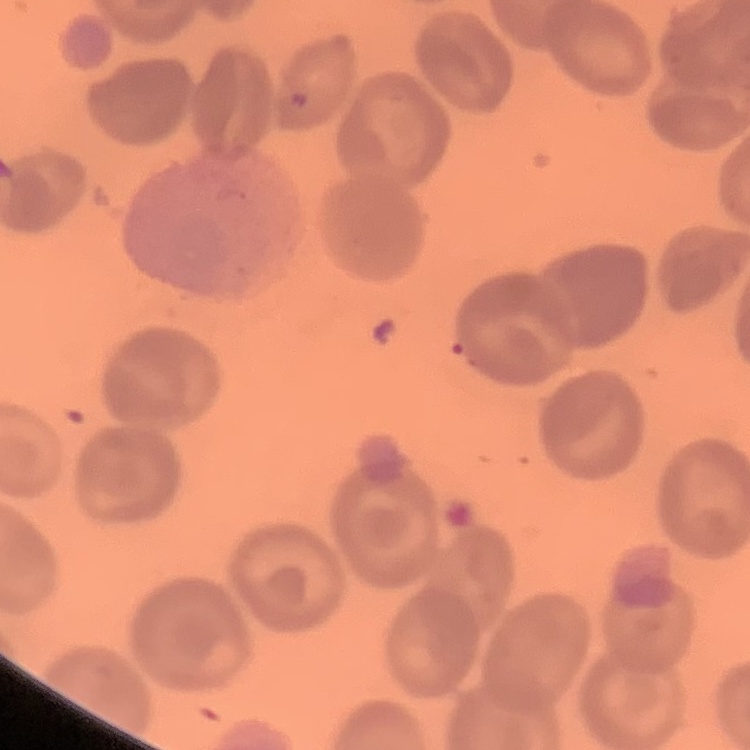
{
  "erythrocyte_morphology": "no rouleaux formation",
  "preparation": "thin blood smear",
  "image_type": "one tile cut from a larger photomicrograph",
  "stain": "Field's or Giemsa"
}